Classify this cell by malaria status.
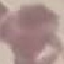
It is uninfected.

{
  "stain": "Giemsa",
  "image_type": "cell patch, automatically extracted from a larger field of view and resized to 64 × 64 pixels",
  "capture": "smartphone through the microscope eyepiece",
  "preparation": "thin smear"
}